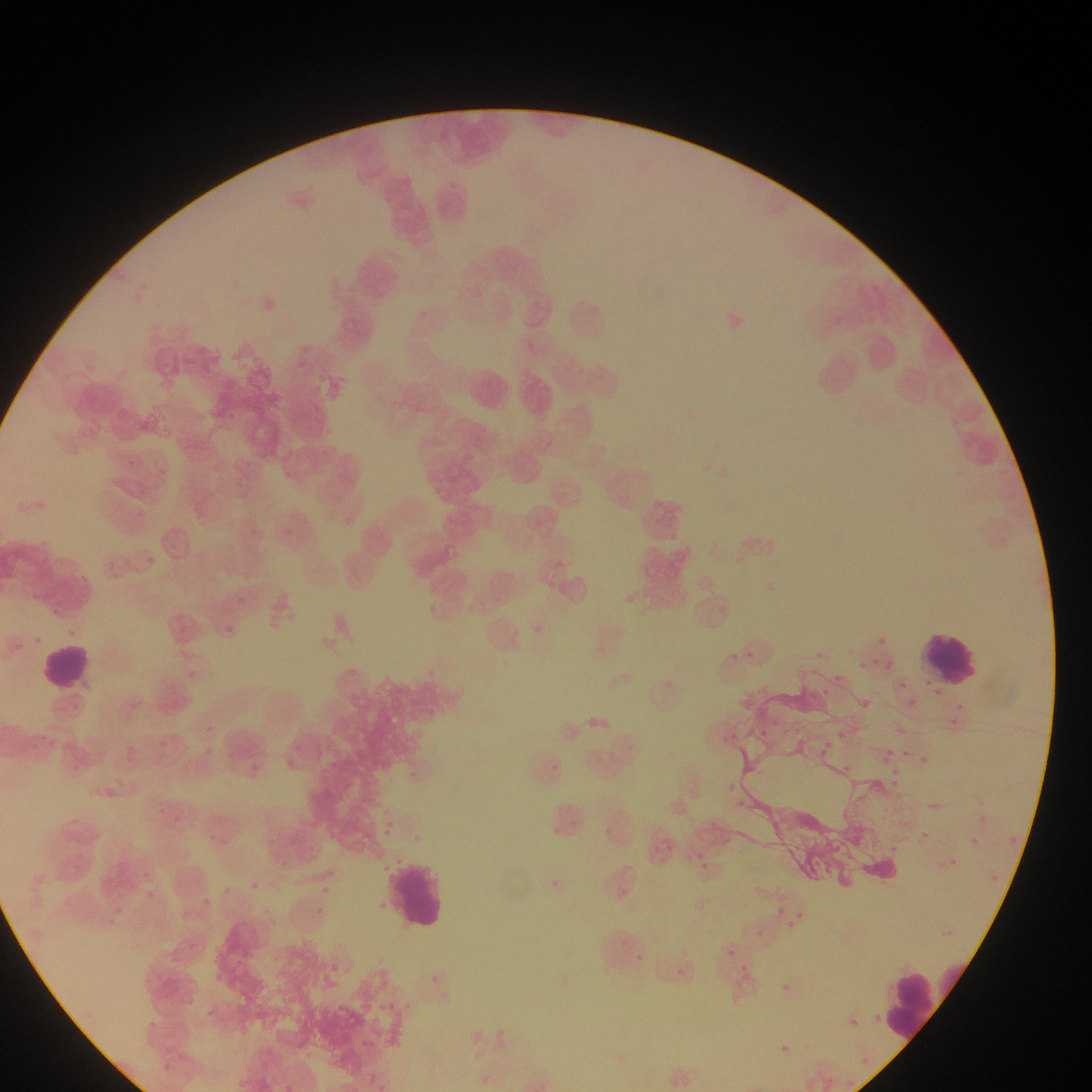

image size = 1092×1092 pixels
preparation = thin blood film
country = Ghana
capture = mobile-phone photograph through a microscope
malaria parasite locations = approximate bounding boxes as left top right bottom in pixels: 226 412 235 421; 284 529 293 537; 148 556 156 564; 30 590 61 611; 614 591 638 604; 237 596 246 605; 715 605 735 618; 533 623 543 630; 225 625 234 634; 59 626 75 639; 33 633 43 645; 875 633 890 651; 14 637 29 659; 747 646 756 659; 813 648 825 657; 729 649 743 670; 876 655 900 676; 858 661 871 676; 833 672 846 688; 666 677 682 694; 897 679 907 691; 817 686 831 698; 900 696 918 707; 860 698 877 715; 954 702 968 712; 587 714 606 725; 946 716 956 727; 769 719 780 727; 200 722 218 735; 839 726 851 745; 758 727 770 745; 730 729 744 742; 724 733 731 746; 826 736 833 747; 157 738 181 754; 202 742 222 764; 882 744 897 760; 904 745 912 760; 311 747 332 766; 820 749 831 754; 921 752 929 763; 288 753 308 777; 142 754 166 770; 881 758 891 768; 247 761 269 784; 64 762 80 775; 549 762 563 774; 844 762 855 774; 888 766 904 778; 888 778 906 787; 725 783 736 792; 105 787 126 811; 734 795 746 810; 162 801 186 824; 970 809 993 833; 70 811 99 838; 706 814 723 833; 371 817 403 842; 605 824 622 834; 547 825 568 843; 921 826 934 838; 205 830 241 851; 328 834 349 847; 1006 834 1021 846; 657 835 681 858; 968 835 990 851; 264 836 280 853; 892 845 908 857; 686 846 708 863; 948 856 971 873; 696 858 722 870; 278 860 303 876; 138 864 153 886; 987 870 1002 881; 544 871 569 886; 244 879 265 899; 314 884 335 899; 144 887 165 906; 216 889 236 900; 197 892 222 917; 780 898 791 913; 113 902 126 919; 180 906 199 931; 786 906 818 938; 311 910 327 925; 749 926 768 944; 727 947 736 956; 634 949 652 963; 325 957 346 982; 736 961 759 986; 675 966 691 985; 427 973 444 993; 783 985 799 999; 377 999 396 1017; 403 1000 419 1013; 868 1005 885 1028; 850 1015 866 1033; 358 1033 375 1050; 775 1040 791 1053; 860 1048 873 1066; 482 1065 495 1088; 367 1070 387 1092; 821 1074 837 1089; 845 1076 857 1092
leukocyte locations = approximate bounding boxes as left top right bottom in pixels: 924 629 983 690; 41 646 90 692; 385 851 450 934; 882 964 950 1048
field of view = single